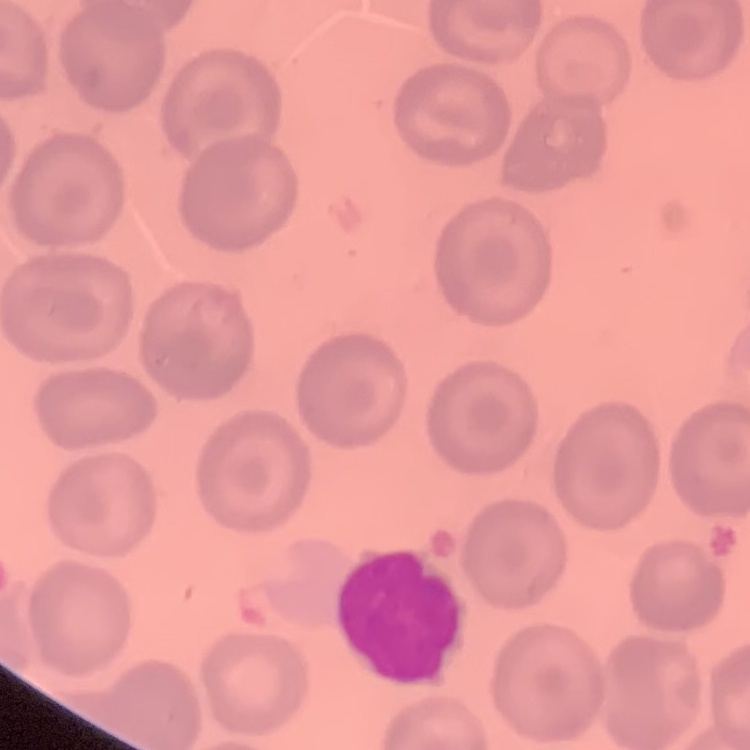
Summary:
  - Red blood cell morphology: no rouleaux formation
  - Stain: Field's or Giemsa
  - Preparation: thin peripheral smear
  - Image type: one tile cut from a larger photomicrograph